Assess this cell for malaria.
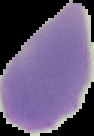

Uninfected.

Summary:
  - Image size: 94×136 pixels
  - Image type: segmented cell region on a black background
  - Preparation: thin blood film